Name the blood parasite species.
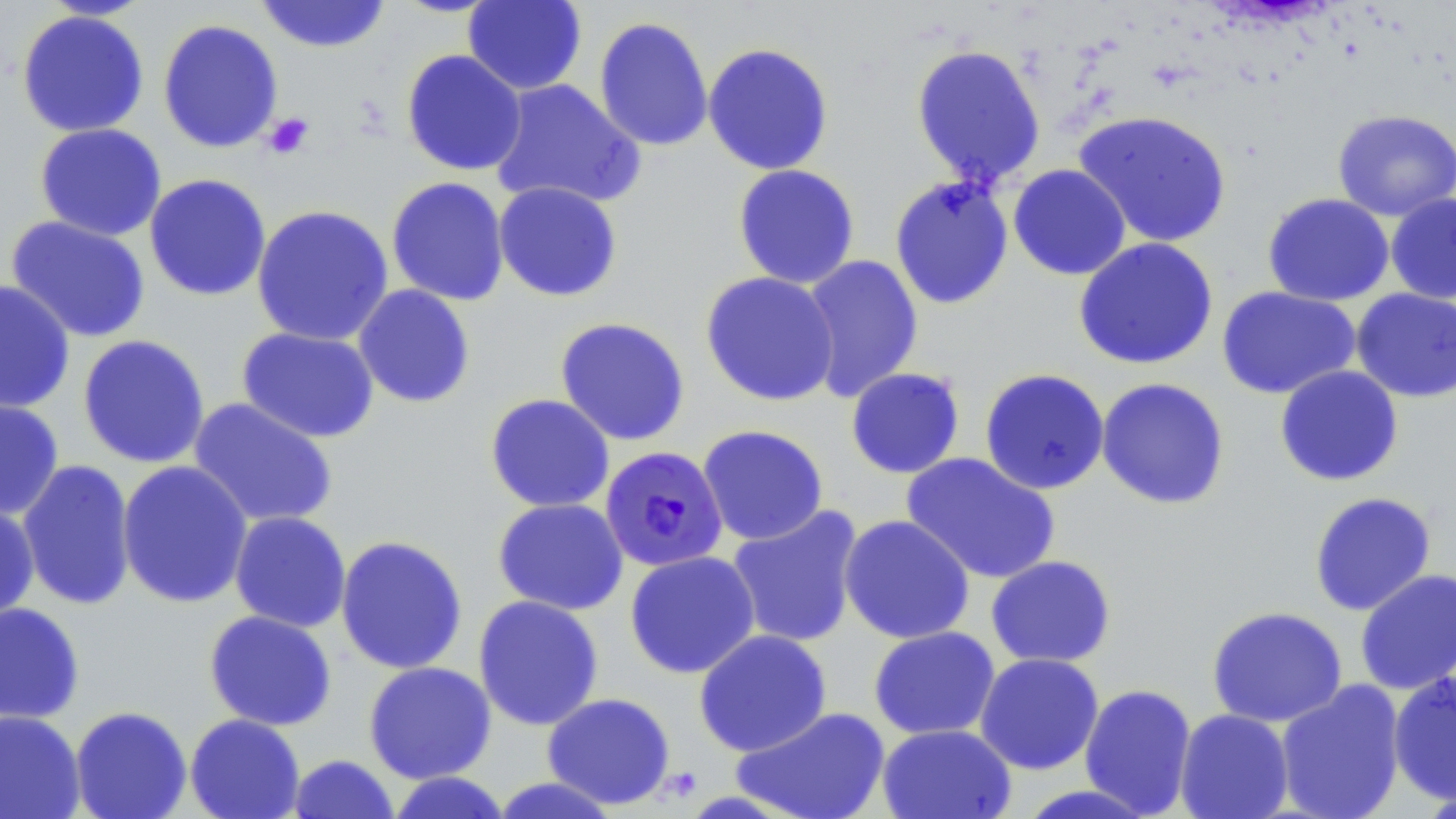
Plasmodium falciparum.

Summary:
  - Coordinate format: approximate bounding boxes as named x1/y1/x2/y2 corners in pixels
  - Uninfected red blood cell locations: (x1=39, y1=0, x2=154, y2=20), (x1=255, y1=0, x2=392, y2=54), (x1=462, y1=1, x2=587, y2=95), (x1=16, y1=9, x2=150, y2=138), (x1=593, y1=16, x2=714, y2=152), (x1=157, y1=19, x2=283, y2=153), (x1=702, y1=42, x2=835, y2=175), (x1=909, y1=43, x2=1047, y2=189), (x1=401, y1=49, x2=527, y2=176), (x1=488, y1=78, x2=645, y2=211), (x1=1072, y1=109, x2=1233, y2=249), (x1=1332, y1=110, x2=1456, y2=222), (x1=33, y1=123, x2=167, y2=241), (x1=732, y1=164, x2=861, y2=289), (x1=1008, y1=164, x2=1131, y2=281), (x1=143, y1=173, x2=272, y2=302), (x1=888, y1=175, x2=1014, y2=310), (x1=386, y1=176, x2=510, y2=306), (x1=494, y1=181, x2=623, y2=302), (x1=1262, y1=193, x2=1394, y2=306), (x1=1385, y1=193, x2=1456, y2=304), (x1=251, y1=204, x2=394, y2=347), (x1=5, y1=215, x2=151, y2=343), (x1=1073, y1=237, x2=1219, y2=371), (x1=799, y1=254, x2=924, y2=403), (x1=700, y1=271, x2=840, y2=407), (x1=0, y1=280, x2=75, y2=414), (x1=353, y1=284, x2=476, y2=408), (x1=1217, y1=286, x2=1361, y2=400), (x1=1350, y1=288, x2=1456, y2=403), (x1=554, y1=316, x2=690, y2=446), (x1=236, y1=326, x2=380, y2=444), (x1=77, y1=334, x2=210, y2=469), (x1=1274, y1=365, x2=1404, y2=487), (x1=846, y1=367, x2=965, y2=479), (x1=979, y1=368, x2=1110, y2=495), (x1=1096, y1=377, x2=1230, y2=510), (x1=485, y1=393, x2=615, y2=513), (x1=0, y1=397, x2=65, y2=521), (x1=187, y1=397, x2=338, y2=529), (x1=697, y1=424, x2=829, y2=545), (x1=900, y1=452, x2=1061, y2=585), (x1=17, y1=459, x2=136, y2=611), (x1=117, y1=460, x2=254, y2=609), (x1=1308, y1=491, x2=1437, y2=616), (x1=492, y1=498, x2=629, y2=615), (x1=0, y1=500, x2=40, y2=622), (x1=726, y1=505, x2=864, y2=648), (x1=229, y1=511, x2=352, y2=632), (x1=839, y1=514, x2=975, y2=644), (x1=335, y1=534, x2=468, y2=675), (x1=624, y1=550, x2=761, y2=679), (x1=985, y1=555, x2=1117, y2=668), (x1=1354, y1=568, x2=1456, y2=695), (x1=473, y1=595, x2=604, y2=731), (x1=0, y1=602, x2=85, y2=725), (x1=1206, y1=606, x2=1348, y2=728), (x1=203, y1=610, x2=337, y2=731), (x1=868, y1=626, x2=1000, y2=740), (x1=693, y1=629, x2=832, y2=757), (x1=975, y1=652, x2=1104, y2=775), (x1=363, y1=661, x2=497, y2=784), (x1=1387, y1=671, x2=1456, y2=806), (x1=1275, y1=680, x2=1407, y2=819), (x1=1079, y1=683, x2=1198, y2=817), (x1=542, y1=692, x2=676, y2=810), (x1=69, y1=705, x2=192, y2=819), (x1=732, y1=706, x2=891, y2=819), (x1=1175, y1=709, x2=1294, y2=819), (x1=0, y1=710, x2=86, y2=819), (x1=184, y1=713, x2=305, y2=819), (x1=877, y1=723, x2=1016, y2=819), (x1=287, y1=754, x2=400, y2=819), (x1=384, y1=771, x2=513, y2=818), (x1=487, y1=775, x2=622, y2=818), (x1=1012, y1=783, x2=1163, y2=818)
  - Platelet locations: (x1=262, y1=112, x2=315, y2=160)
  - Plasmodium falciparum-infected red blood cell locations: (x1=600, y1=446, x2=728, y2=572)
  - Stain: May-Grünwald-Giemsa
  - Magnification: 1000x
  - Preparation: thin blood film
  - Modality: light microscopy
  - Image size: 1456×819 pixels
  - Field of view: one of a larger specimen